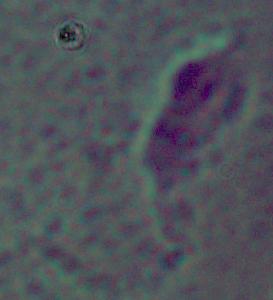 Photomicrograph. A Leishmania parasite is seen. Captured at 1000x magnification.